Outline each blood parasite and name the species.
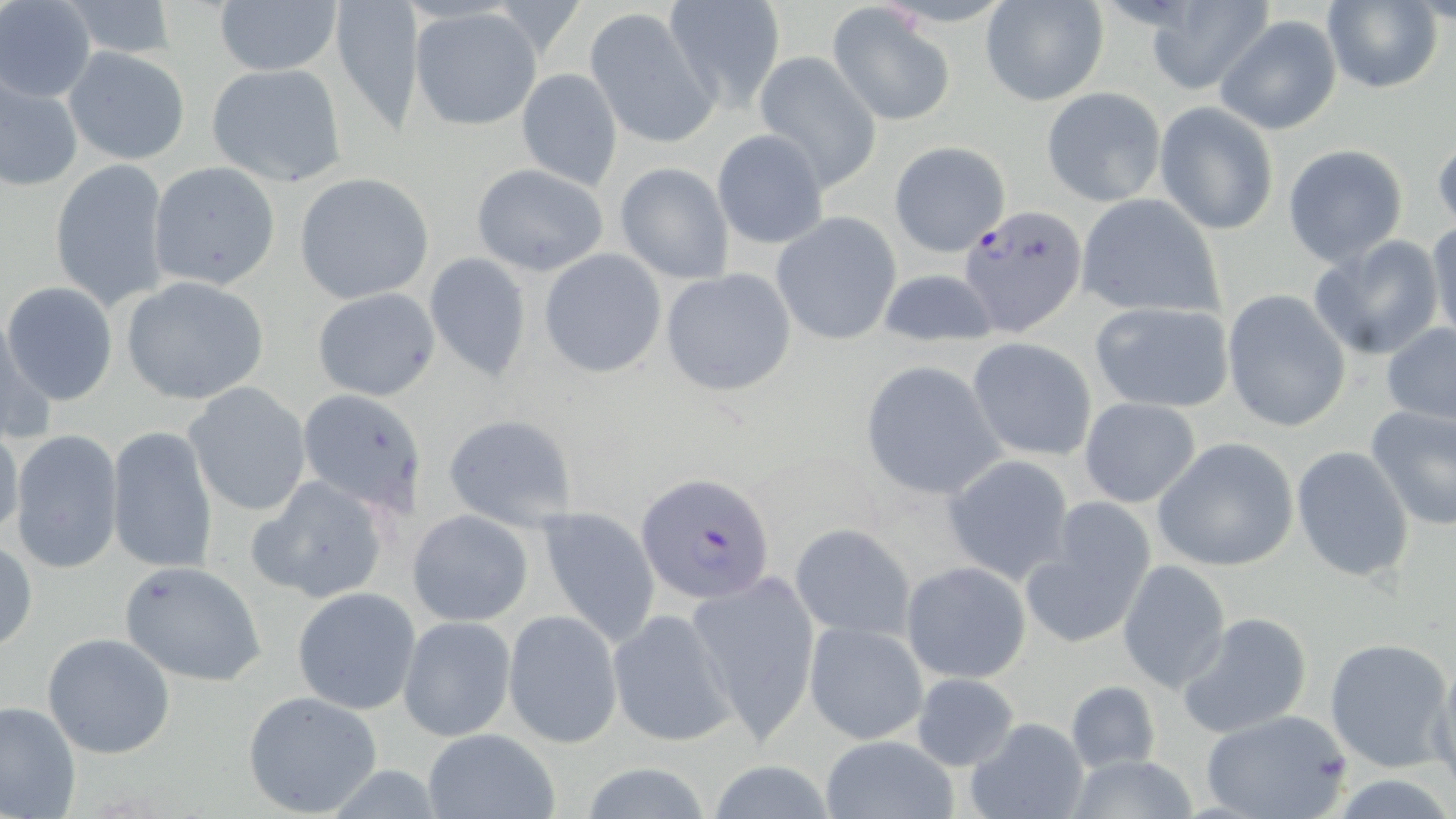
Approximate bounding boxes as [x1, y1, x2, y2] in pixels.
Plasmodium falciparum-infected red blood cells: [958, 204, 1086, 334], [635, 473, 777, 606].
No Plasmodium ovale, Plasmodium malariae, Plasmodium vivax, Babesia divergens, or Trypanosoma brucei observed.

slide_level_diagnosis: Plasmodium falciparum
field_of_view: single
preparation: thin blood film
stain: May-Grünwald-Giemsa
modality: optical microscopy
uninfected_red_blood_cell_locations: 'approximate bounding boxes as [x1, y1, x2, y2] in pixels: [56, 0, 182, 63], [329, 0, 424, 133], [661, 0, 787, 110], [0, 1, 97, 103], [211, 1, 340, 77], [1319, 1, 1443, 94], [979, 2, 1108, 108], [1139, 4, 1272, 94], [825, 6, 955, 126], [409, 7, 542, 131], [583, 8, 718, 148], [1216, 14, 1342, 134], [64, 47, 190, 165], [752, 51, 881, 194], [208, 63, 347, 188], [515, 68, 623, 192], [0, 70, 83, 194], [1041, 87, 1166, 207], [1155, 103, 1278, 236], [713, 131, 828, 250], [1431, 131, 1455, 231], [888, 141, 1011, 257], [1282, 144, 1408, 267], [49, 158, 171, 312], [147, 162, 281, 289], [469, 162, 610, 277], [614, 163, 733, 283], [294, 173, 436, 305], [1074, 194, 1226, 320], [771, 212, 902, 345], [1426, 219, 1456, 344], [1308, 235, 1445, 360], [538, 249, 667, 378], [425, 252, 535, 381], [659, 267, 797, 397], [875, 267, 997, 347], [120, 275, 269, 405], [3, 281, 118, 406], [310, 287, 442, 401], [1221, 289, 1350, 433], [1087, 301, 1236, 413], [2, 315, 55, 448], [1380, 322, 1456, 426], [967, 337, 1097, 461], [860, 361, 1005, 502], [183, 382, 312, 518], [298, 389, 428, 512], [1078, 397, 1201, 507], [1365, 404, 1456, 531], [442, 413, 578, 531], [0, 417, 25, 547], [107, 426, 218, 575], [9, 430, 124, 575], [1154, 437, 1300, 572], [1291, 445, 1415, 584], [942, 454, 1075, 585], [247, 474, 392, 605], [1021, 503, 1156, 648], [538, 506, 662, 650], [408, 509, 534, 626], [790, 523, 917, 643], [0, 539, 38, 654], [1118, 559, 1230, 692], [117, 560, 267, 687], [901, 561, 1033, 683], [687, 571, 820, 742], [291, 586, 420, 716], [607, 606, 734, 747], [503, 610, 622, 748], [1175, 611, 1314, 740], [398, 616, 516, 743], [803, 619, 929, 747], [42, 632, 176, 760], [1323, 636, 1453, 772], [1429, 655, 1455, 799], [909, 672, 1021, 771], [1064, 679, 1161, 774], [243, 690, 384, 817], [0, 700, 80, 819], [1198, 709, 1353, 819], [964, 717, 1090, 819], [423, 727, 558, 819], [820, 735, 959, 819], [1063, 756, 1204, 818], [700, 759, 844, 819], [572, 760, 720, 819]'
magnification: 1000x
image_size: 1456×819 pixels